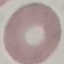

Summary:
  - Malaria status: uninfected
  - Preparation: thin blood film
  - Capture: smartphone through the microscope eyepiece
  - Stain: Giemsa
  - Image type: automatically extracted cell patch, resized to 64 × 64 pixels